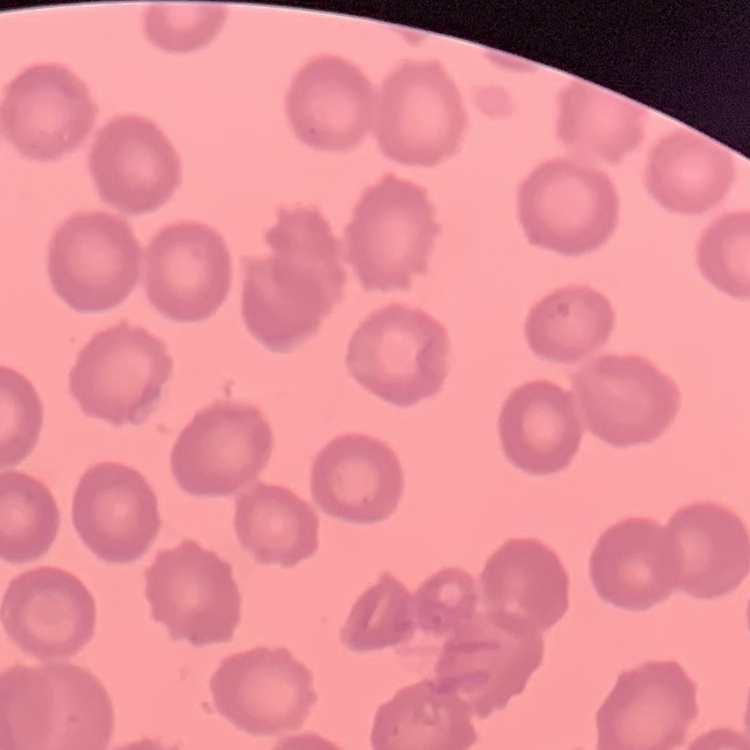
{
  "erythrocyte_morphology": "no rouleaux formation",
  "image_type": "one tile cut from a larger photomicrograph",
  "stain": "Field's or Giemsa",
  "preparation": "thin blood film"
}